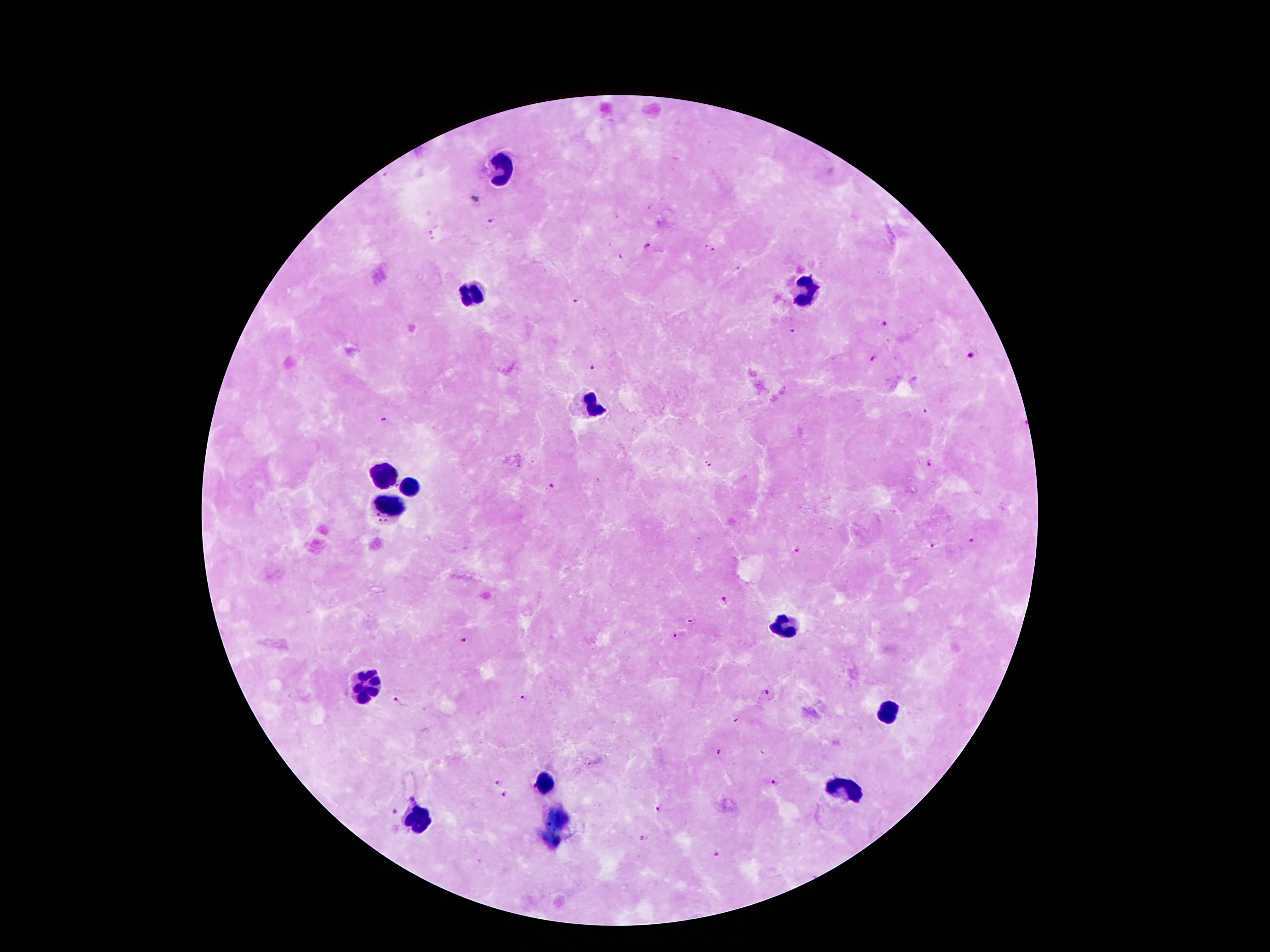

{
  "leukocyte_locations": "approximate centers as [x, y] in pixels: [499, 165], [809, 289], [471, 295], [587, 404], [385, 472], [408, 488], [391, 509], [780, 625], [366, 682], [883, 711], [547, 785], [843, 791], [419, 816]",
  "malaria_parasite_locations": "approximate centers as [x, y] in pixels: [491, 221], [707, 243], [645, 244], [713, 249], [620, 257], [739, 266], [575, 301], [886, 324], [793, 331], [971, 357], [872, 359], [593, 367], [926, 410], [384, 420], [708, 464], [926, 465], [551, 486], [971, 539], [931, 545], [797, 551], [724, 599], [691, 618], [675, 635], [465, 640], [764, 693], [524, 696], [396, 700], [735, 722], [719, 752], [498, 783], [773, 784], [505, 793], [656, 808], [394, 810], [644, 837], [717, 854]",
  "magnification": "100x",
  "field_of_view": "single",
  "patient_malaria_status": "infected with Plasmodium falciparum",
  "capture": "smartphone camera through the microscope eyepiece",
  "preparation": "thick blood smear",
  "image_size": "1270×952 pixels",
  "stain": "Giemsa"
}